Classify this cell by malaria status.
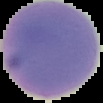

Uninfected.

Summary:
  - Image size: 103×103 pixels
  - Image type: segmented cell region with the area outside set to black
  - Preparation: thin blood smear